Give the position of every malaria parasite.
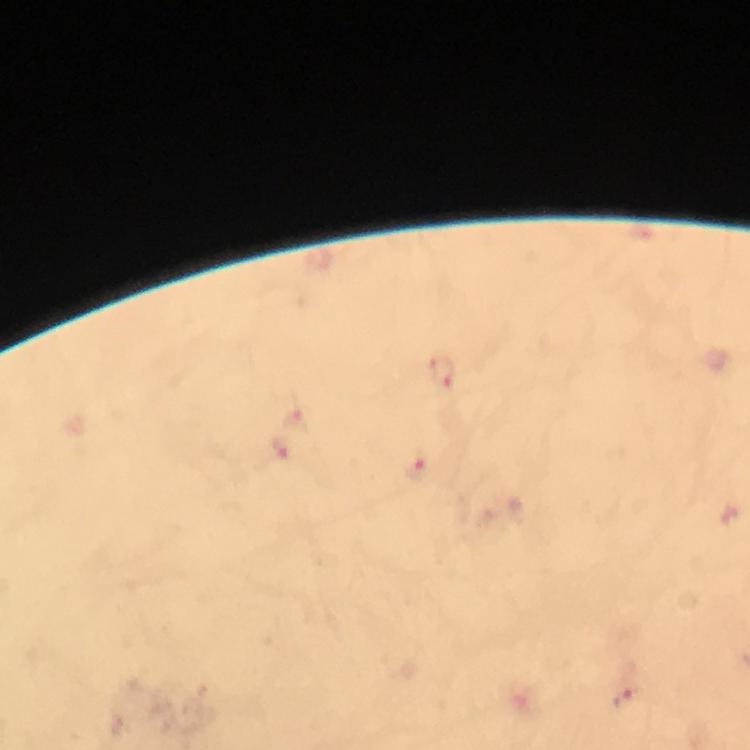

Approximate centers as (x, y) in pixels.
Malaria parasites: (444, 374), (298, 420), (282, 452), (420, 466), (623, 699).

Giemsa-stained preparation. From a malaria diagnostic workup. Cropped region of a single field of view. Smartphone photograph taken through a microscope. At 100x magnification. Immersion oil applied. Thick blood smear. Image is 750×750 pixels.